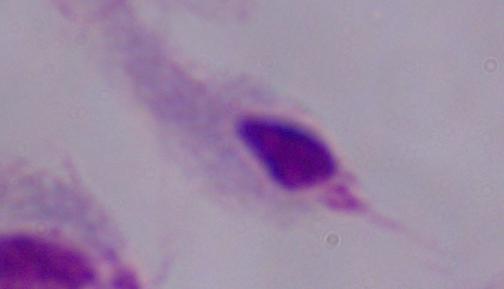
Summary:
  - Modality: photomicrograph
  - Identification: trichomonad
  - Magnification: 1000x